Point out each Plasmodium parasite.
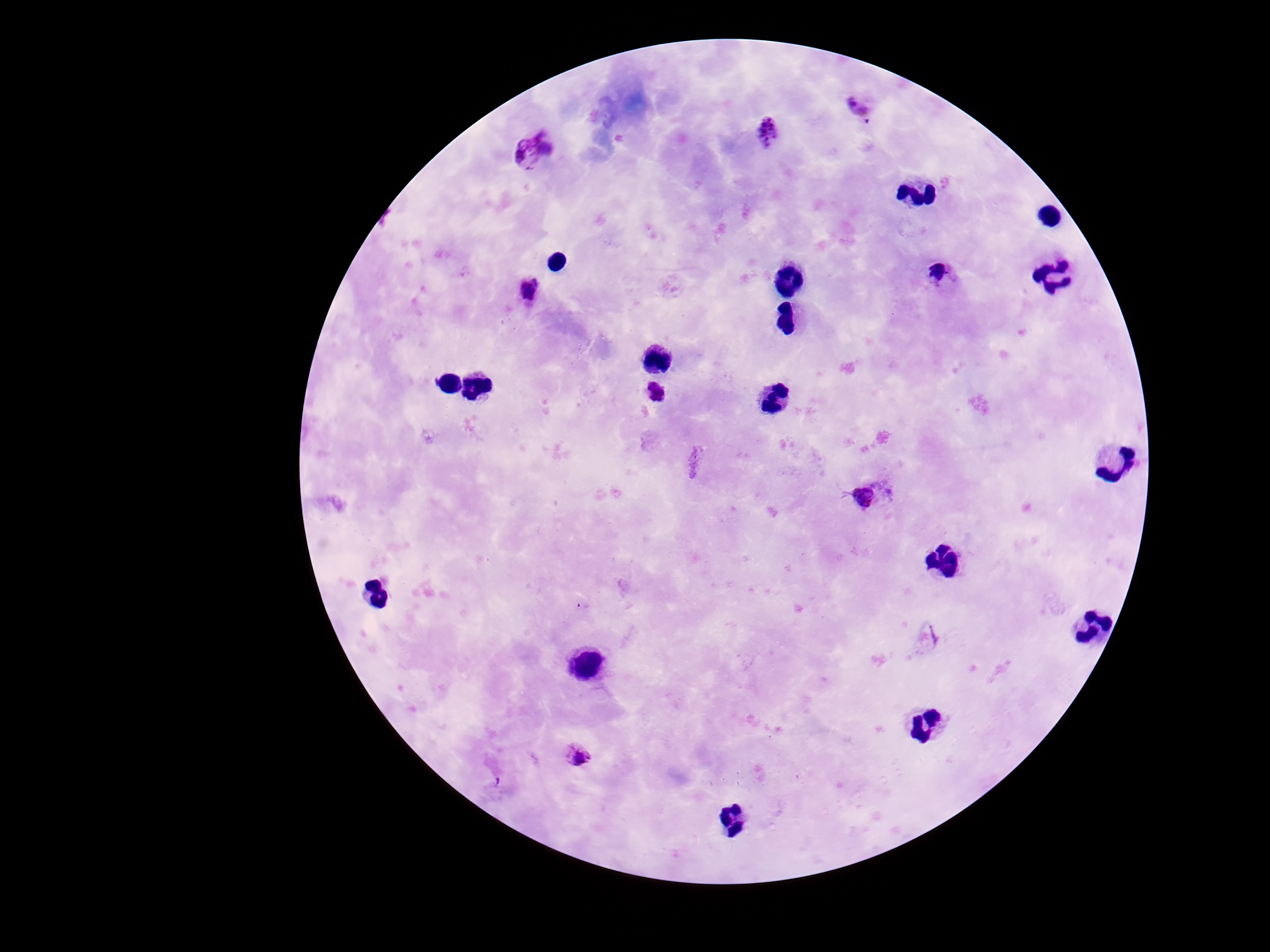

Approximate centers as (x, y) in pixels.
Plasmodium parasites: (860, 106), (770, 130), (524, 156), (939, 271), (531, 289), (656, 392), (862, 499), (583, 605), (579, 753).

Summary:
  - Stain: Giemsa
  - Image size: 1270×952 pixels
  - Preparation: thick peripheral-blood smear
  - Capture: smartphone camera through the microscope eyepiece
  - Field of view: one from this slide
  - Patient malaria status: infected
  - Magnification: 100x